Give the position of every leukocyte visible.
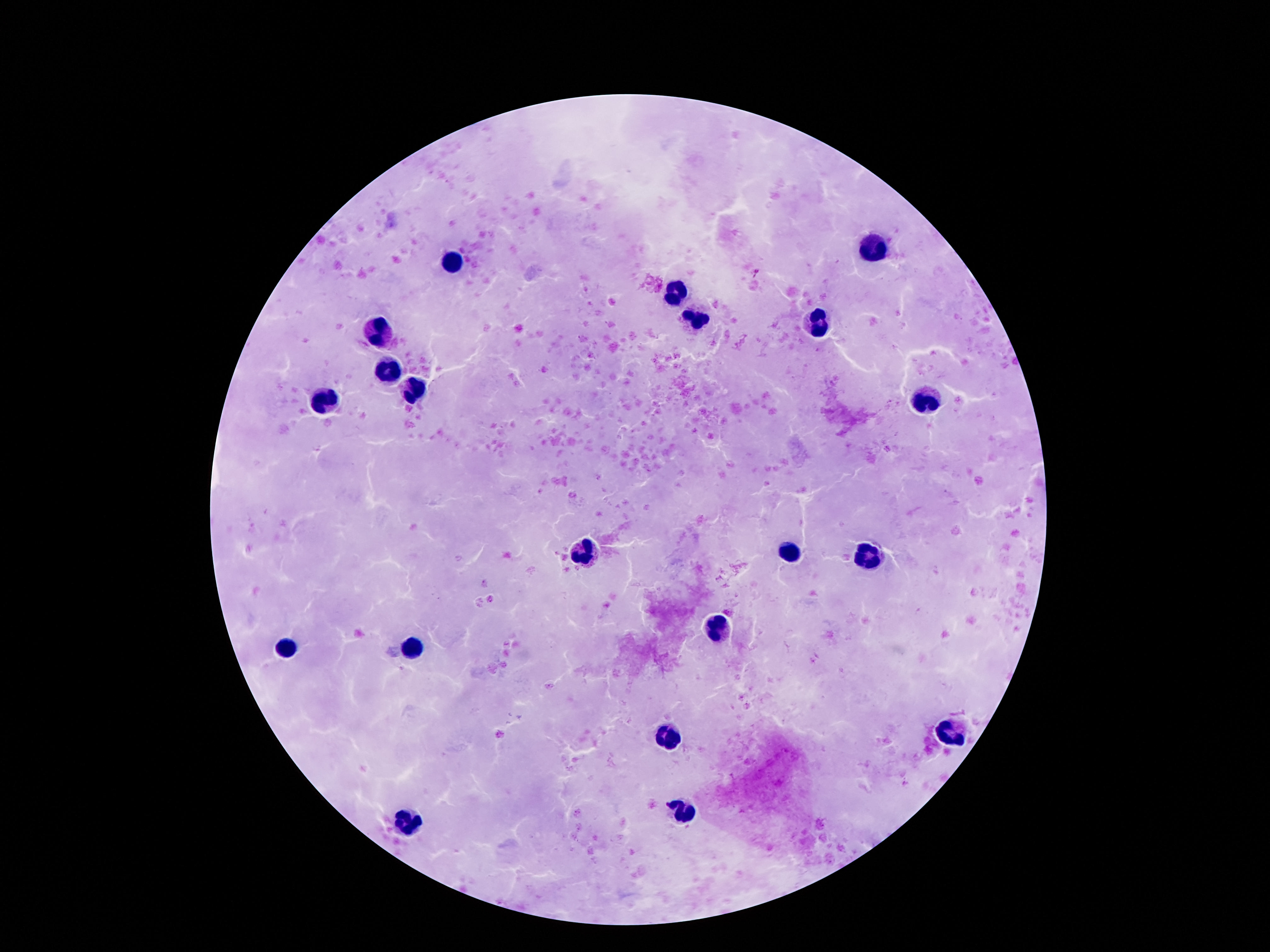
Approximate centers as {x, y} in pixels.
Leukocytes: {870, 246}, {452, 260}, {673, 293}, {695, 321}, {813, 321}, {375, 330}, {387, 369}, {412, 389}, {323, 401}, {925, 401}, {584, 546}, {786, 548}, {870, 555}, {720, 625}, {287, 648}, {414, 652}, {952, 734}, {666, 737}, {679, 809}, {405, 819}.

One field from this slide. Thick peripheral-blood smear. Patient malaria status: negative. Giemsa-stained preparation. Image is 1270×952 pixels. Smartphone photograph taken through the microscope eyepiece. 100x magnification.